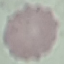
Result: no malaria parasites seen. Thin blood film. Giemsa stain. Photographed with a smartphone camera at the microscope eyepiece. Cell patch, automatically extracted from a larger field of view and resized to 64 × 64 pixels.